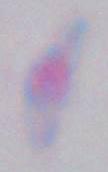

Summary:
  - Modality: micrograph
  - Magnification: 1000x
  - Identification: Toxoplasma gondii